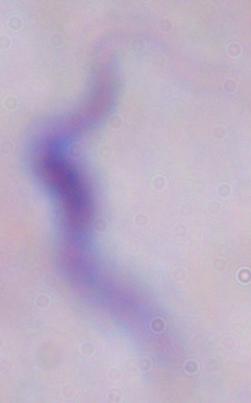

Captured at 1000x magnification. A trypanosome is seen. Photomicrograph.